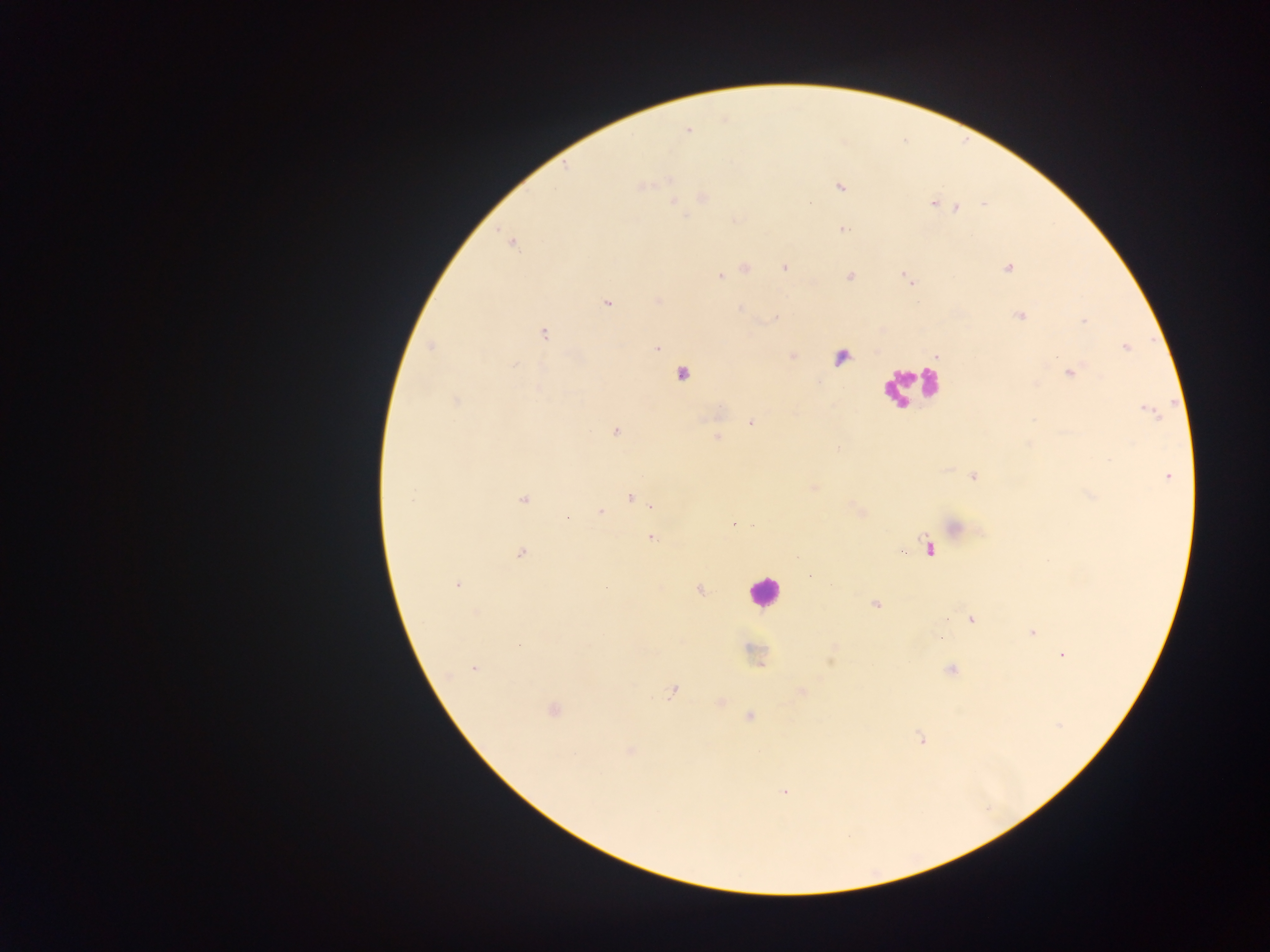
Approximate centers as x y in pixels.
Summary:
  - Leukocyte locations: 907 385; 763 591
  - Plasmodium parasite locations: 687 130; 641 186; 840 187; 703 198; 674 201; 810 204; 932 204; 983 204; 956 208; 684 216; 842 229; 511 242; 784 267; 745 268; 1007 268; 721 276; 849 277; 906 278; 607 303; 739 309; 1020 316; 776 318; 1084 321; 543 335; 431 347; 1126 347; 657 348; 793 357; 514 365; 681 373; 1070 373; 456 401; 1149 412; 750 422; 615 431; 716 438; 972 477; 1167 477; 814 488; 1091 494; 630 498; 411 499; 523 500; 652 506; 600 512; 568 517; 954 528; 653 538; 928 548; 521 552; 810 576; 457 585; 700 590; 875 604; 476 612; 971 620; 1032 633; 753 653; 1062 655; 475 668; 951 670; 672 692; 801 692; 553 709; 749 717; 920 738; 630 751; 785 792
  - Country: Ghana
  - Image size: 1270×952 pixels
  - Field of view: single
  - Preparation: thick blood smear
  - Capture: mobile-phone photograph through a microscope